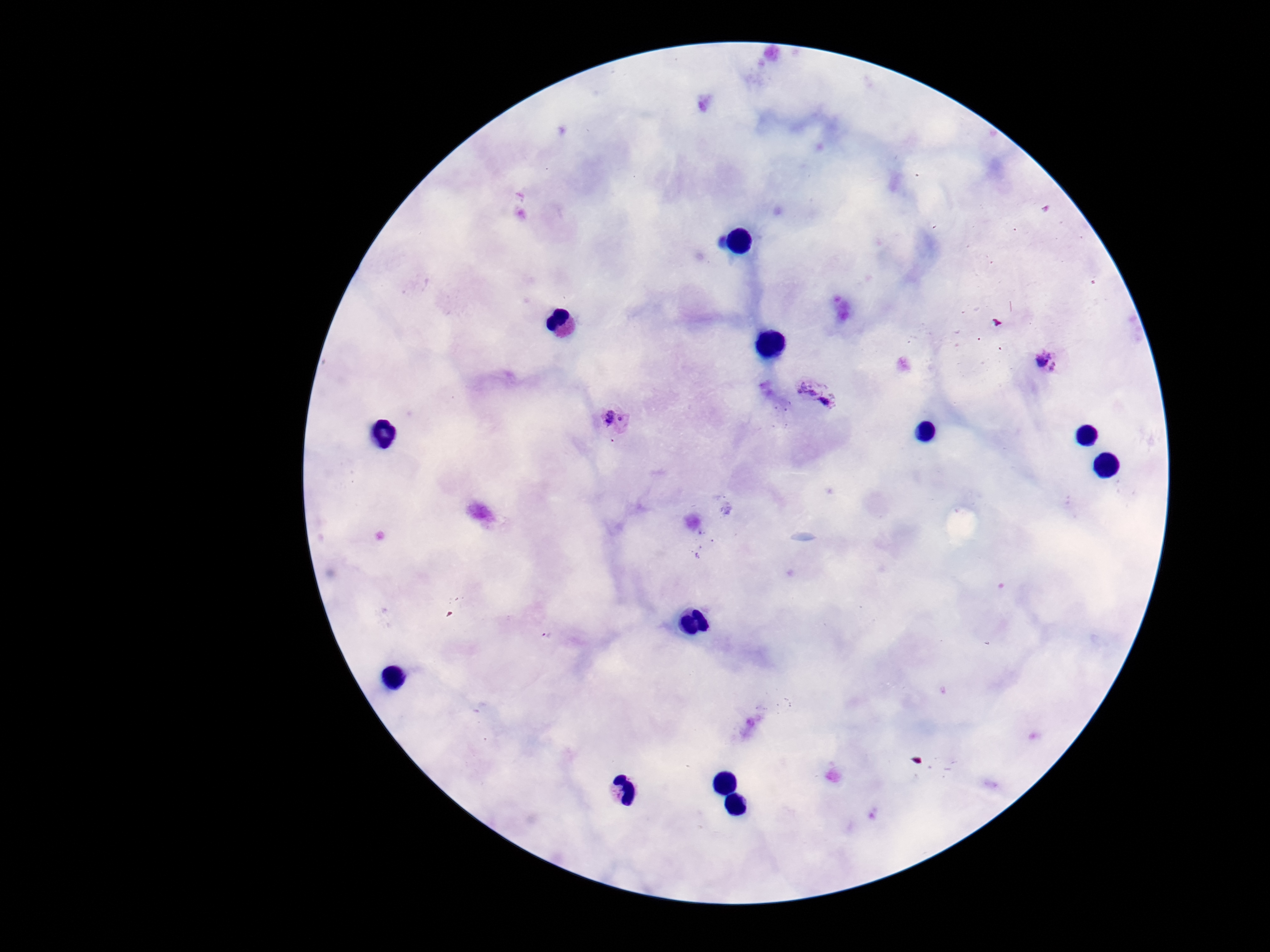
Approximate centers as {x, y} in pixels.
Summary:
  - Plasmodium parasite locations: {1049, 361}, {818, 394}, {613, 419}
  - Magnification: 100x
  - Preparation: thick blood film
  - Capture: smartphone camera through the microscope eyepiece
  - Image size: 1270×952 pixels
  - Stain: Giemsa
  - Patient malaria status: positive
  - Field of view: one from this slide